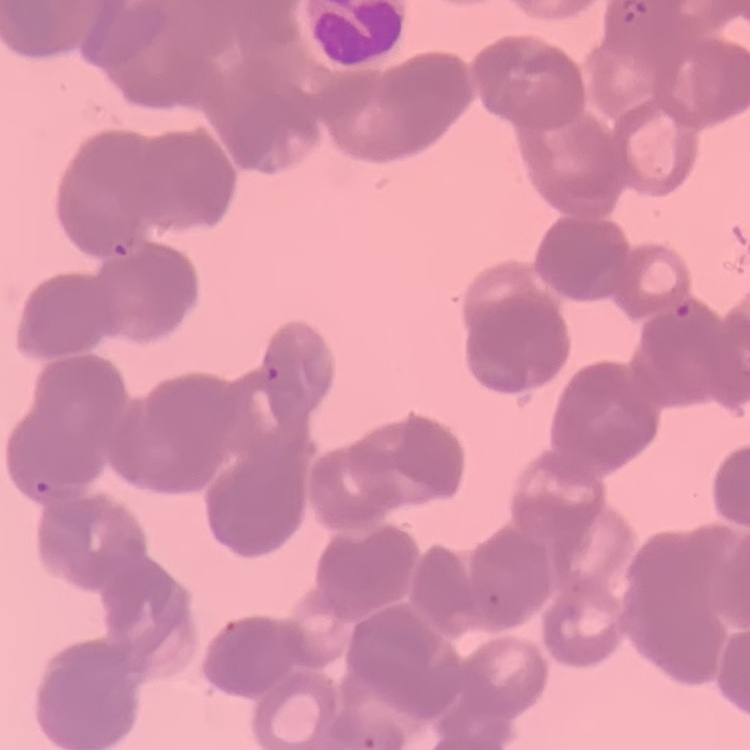
red blood cell morphology = rouleaux formation
image type = square crop of a larger photomicrograph
stain = Field's or Giemsa
preparation = thin blood film